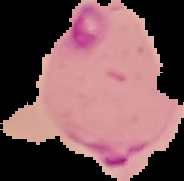

Summary:
  - Preparation: thin blood film
  - Image size: 184×181 pixels
  - Result: Plasmodium parasites identified
  - Image type: segmented cell region with the area outside set to black